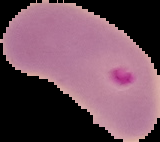
preparation: thin blood film
result: Plasmodium parasites identified
image_type: segmented cell region with the area outside set to black
image_size: 160×142 pixels